Assess the morphology of the erythrocytes.
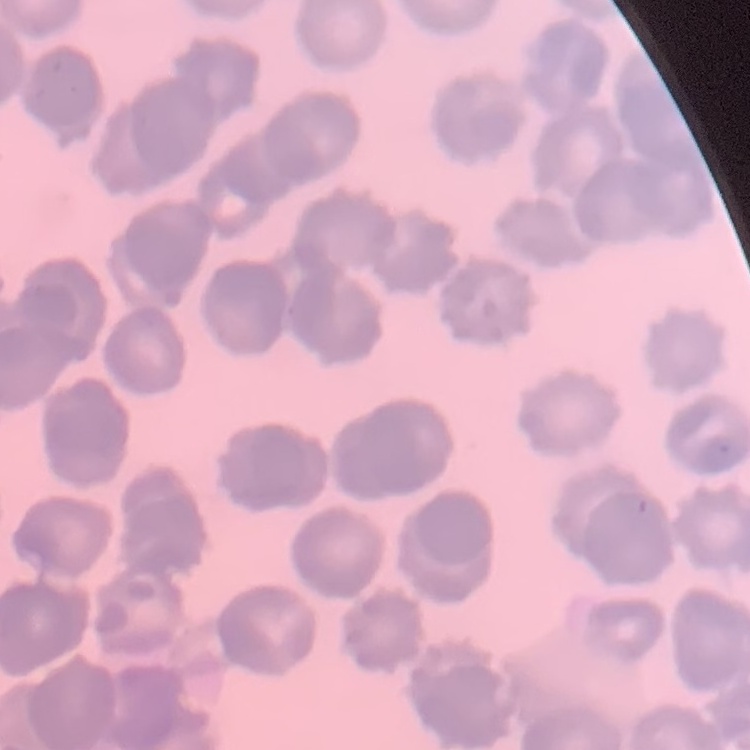

They show rouleaux formation.

preparation = thin peripheral smear
image type = one tile cut from a larger photomicrograph
stain = Field's or Giemsa